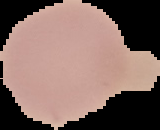

Summary:
  - Image type: segmented cell region on a black background
  - Result: no malaria parasites seen
  - Image size: 160×130 pixels
  - Preparation: thin blood smear